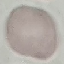

Summary:
  - Result: no malaria parasites detected
  - Capture: smartphone camera at the microscope eyepiece
  - Preparation: thin blood smear
  - Image type: cell patch, automatically extracted from a larger field of view and resized to 64 × 64 pixels
  - Stain: Giemsa